Assess the morphology of the red blood cells.
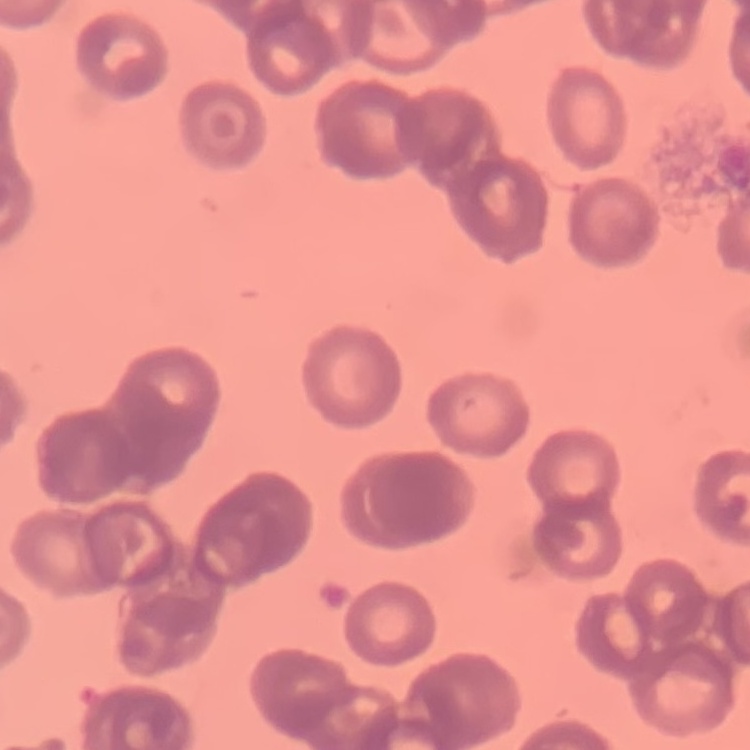
They show rouleaux formation.

Summary:
  - Preparation: thin blood film
  - Stain: Field's or Giemsa
  - Image type: square crop of a larger photomicrograph